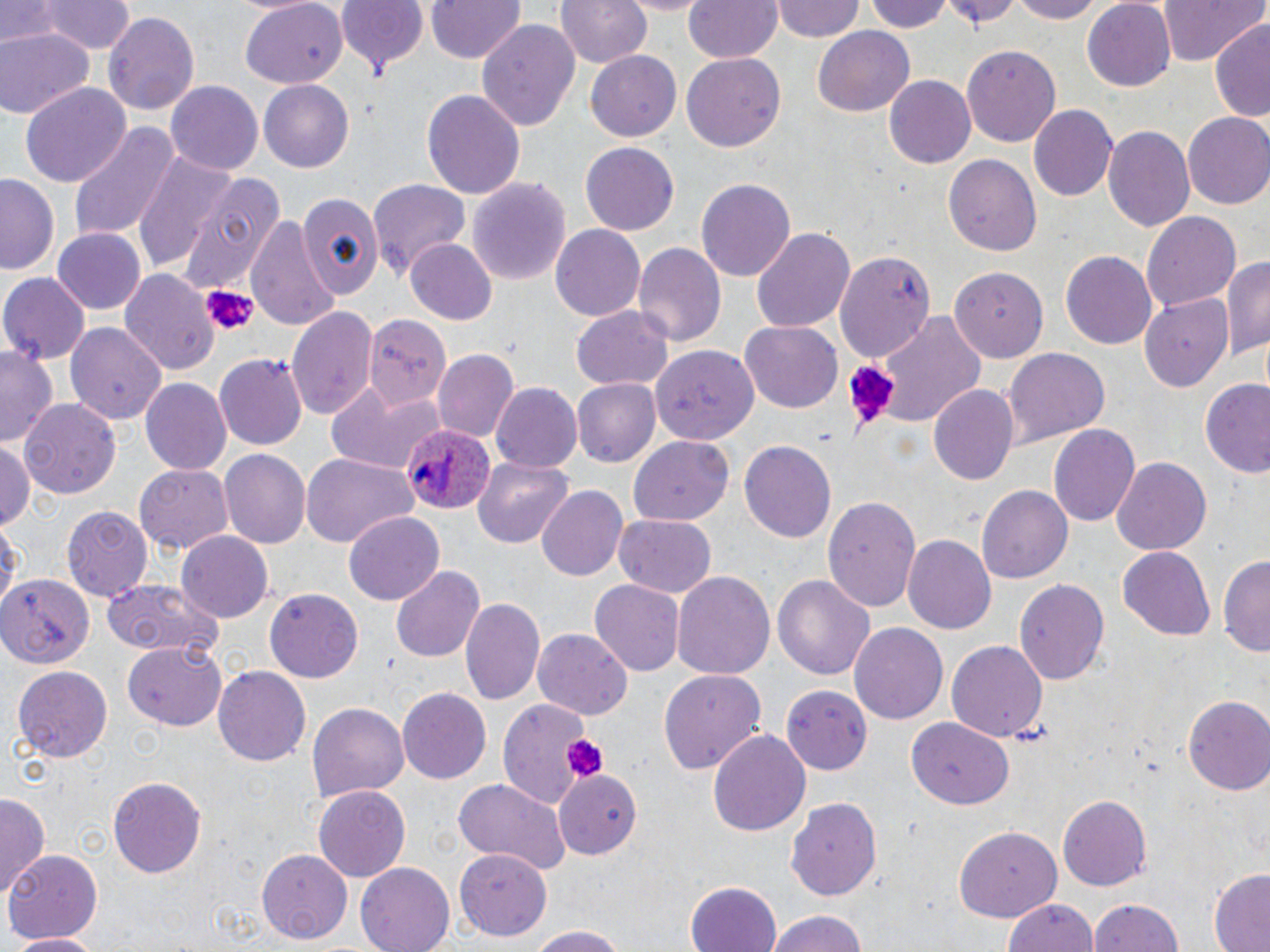 Approximate bounding boxes as (x1, y1, x2, y2) in pixels. Platelet locations: (198, 282, 259, 340), (842, 360, 896, 428), (559, 732, 606, 780). Plasmodium ovale-infected red blood cell locations: (403, 421, 496, 518). Uninfected red blood cell locations: (0, 0, 63, 46), (41, 0, 135, 56), (333, 0, 429, 77), (422, 0, 526, 65), (558, 0, 652, 70), (619, 0, 710, 14), (683, 0, 783, 64), (772, 0, 863, 43), (865, 0, 955, 32), (942, 0, 1018, 29), (1006, 0, 1106, 23), (1083, 0, 1179, 89), (1162, 0, 1264, 68), (237, 1, 347, 87), (105, 13, 198, 115), (476, 19, 581, 134), (1211, 22, 1270, 123), (0, 27, 95, 119), (814, 28, 914, 115), (961, 44, 1060, 146), (584, 49, 685, 142), (682, 52, 786, 152), (883, 76, 974, 169), (166, 80, 262, 172), (259, 80, 354, 172), (20, 83, 130, 188), (420, 89, 526, 200), (1027, 104, 1117, 204), (1183, 113, 1270, 208), (67, 120, 178, 243), (1103, 123, 1195, 232), (580, 142, 679, 236), (130, 149, 235, 275), (944, 154, 1041, 257), (173, 171, 285, 295), (1, 173, 62, 276), (468, 176, 570, 289), (697, 176, 796, 282), (368, 179, 470, 276), (296, 190, 388, 305), (1144, 211, 1241, 311), (246, 213, 341, 333), (550, 224, 645, 322), (751, 226, 854, 336), (54, 228, 145, 314), (405, 239, 497, 325), (632, 242, 725, 352), (835, 248, 937, 364), (1060, 252, 1159, 348), (1218, 256, 1270, 362), (951, 263, 1053, 362), (119, 267, 218, 375), (1, 272, 89, 364), (1141, 295, 1230, 391), (288, 305, 378, 418), (571, 306, 675, 390), (364, 313, 449, 409), (871, 314, 988, 432), (740, 321, 843, 413), (66, 322, 168, 424), (0, 345, 58, 446), (649, 345, 759, 441), (1004, 345, 1109, 443), (433, 351, 519, 443), (214, 352, 308, 450), (1201, 377, 1270, 480), (140, 379, 231, 475), (572, 379, 660, 468), (327, 381, 444, 474), (491, 383, 581, 474), (930, 385, 1019, 488), (19, 397, 122, 496), (1049, 422, 1140, 528), (631, 435, 735, 524), (739, 438, 836, 539), (0, 439, 35, 531), (218, 449, 309, 550), (300, 452, 416, 550), (1112, 456, 1212, 556), (473, 457, 574, 547), (135, 461, 232, 552), (536, 485, 627, 583), (977, 485, 1071, 586), (823, 494, 922, 609), (60, 504, 150, 599), (344, 512, 444, 605), (613, 515, 717, 598), (0, 519, 20, 618), (178, 530, 274, 621), (903, 535, 996, 635), (1119, 546, 1215, 639), (1218, 552, 1269, 658), (389, 564, 483, 665), (670, 569, 776, 679), (0, 573, 92, 669), (771, 574, 876, 682), (590, 578, 684, 674), (1015, 578, 1109, 687), (100, 579, 224, 657), (264, 588, 363, 682), (460, 596, 544, 704), (849, 622, 948, 726), (534, 630, 630, 721), (947, 640, 1048, 744), (120, 645, 230, 730), (213, 664, 310, 764), (11, 665, 114, 762), (660, 669, 766, 777), (782, 685, 876, 774), (397, 687, 495, 784), (1183, 696, 1270, 796), (497, 698, 593, 810), (308, 701, 409, 800), (907, 716, 1013, 810), (707, 728, 813, 839), (554, 766, 642, 860), (106, 777, 207, 879), (453, 777, 572, 876), (313, 786, 409, 882), (1057, 792, 1152, 890), (0, 793, 49, 900), (786, 794, 883, 901), (957, 828, 1060, 921), (6, 848, 104, 943), (259, 849, 352, 943), (455, 851, 555, 941), (355, 864, 455, 952), (1208, 868, 1270, 952), (686, 881, 784, 952), (1002, 896, 1101, 952), (1089, 897, 1184, 952), (762, 909, 873, 952), (520, 923, 635, 952), (7, 932, 106, 951). Slide-level diagnosis: Plasmodium ovale. One field of a larger specimen. Image is 1270×952 pixels. 1000x magnification. Thin blood smear. Optical microscopy. May-Grünwald-Giemsa-stained preparation.